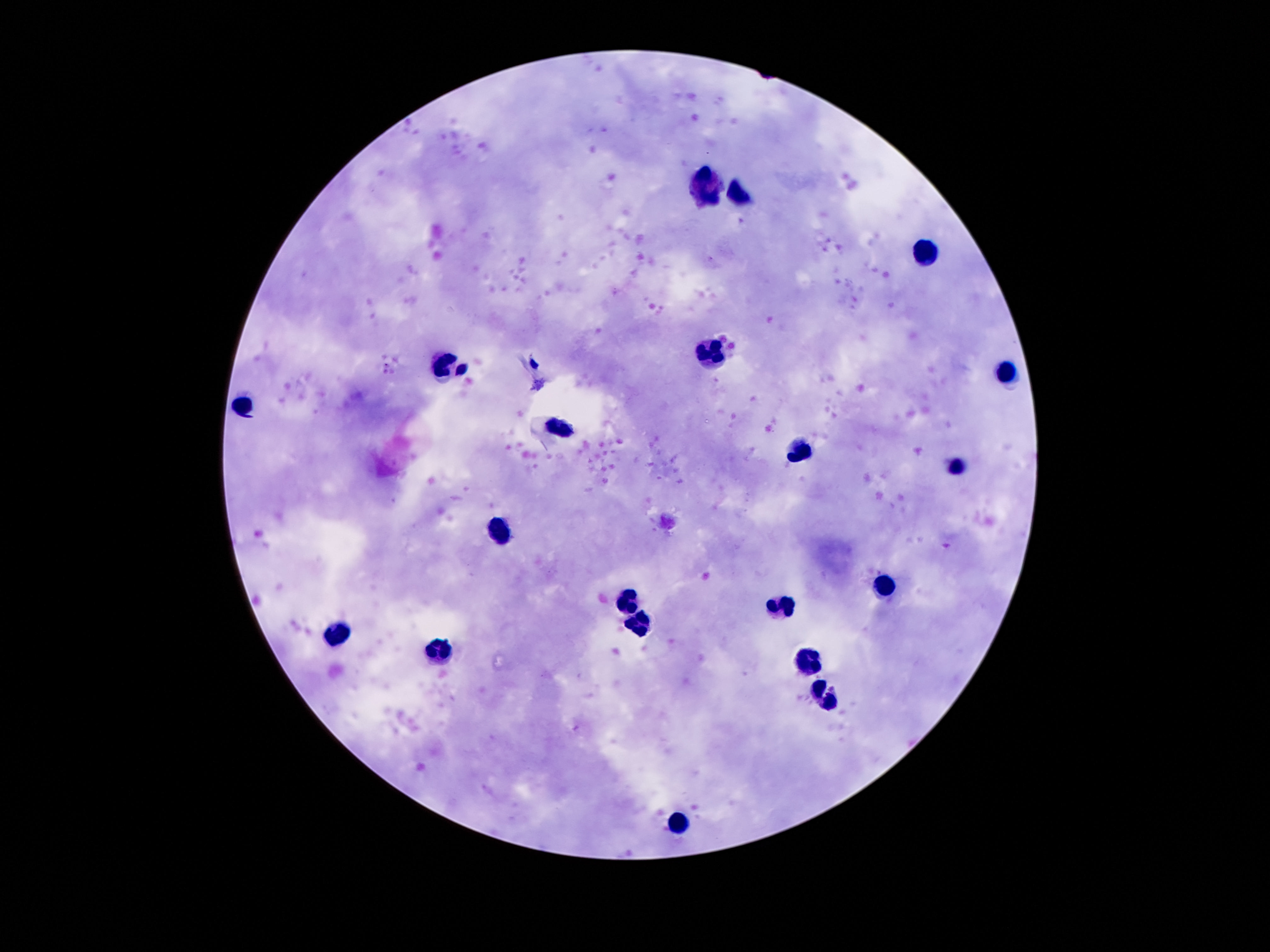
Approximate centers as [x, y] in pixels.
Summary:
  - Leukocyte locations: [706, 183], [742, 194], [925, 255], [714, 353], [449, 363], [1004, 375], [243, 404], [564, 428], [798, 451], [958, 466], [498, 530], [884, 586], [627, 599], [785, 607], [642, 626], [339, 632], [440, 650], [811, 659], [826, 696], [678, 823]
  - Field of view: one from this slide
  - Preparation: thick blood smear
  - Patient malaria status: not infected
  - Magnification: 100x
  - Image size: 1270×952 pixels
  - Stain: Giemsa
  - Capture: smartphone camera through the microscope eyepiece